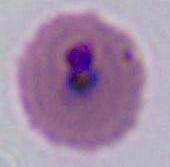

magnification = 400x or 1000x
modality = photomicrograph
identification = Plasmodium